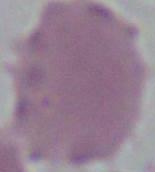

magnification: 1000x
modality: photomicrograph
identification: red blood cell